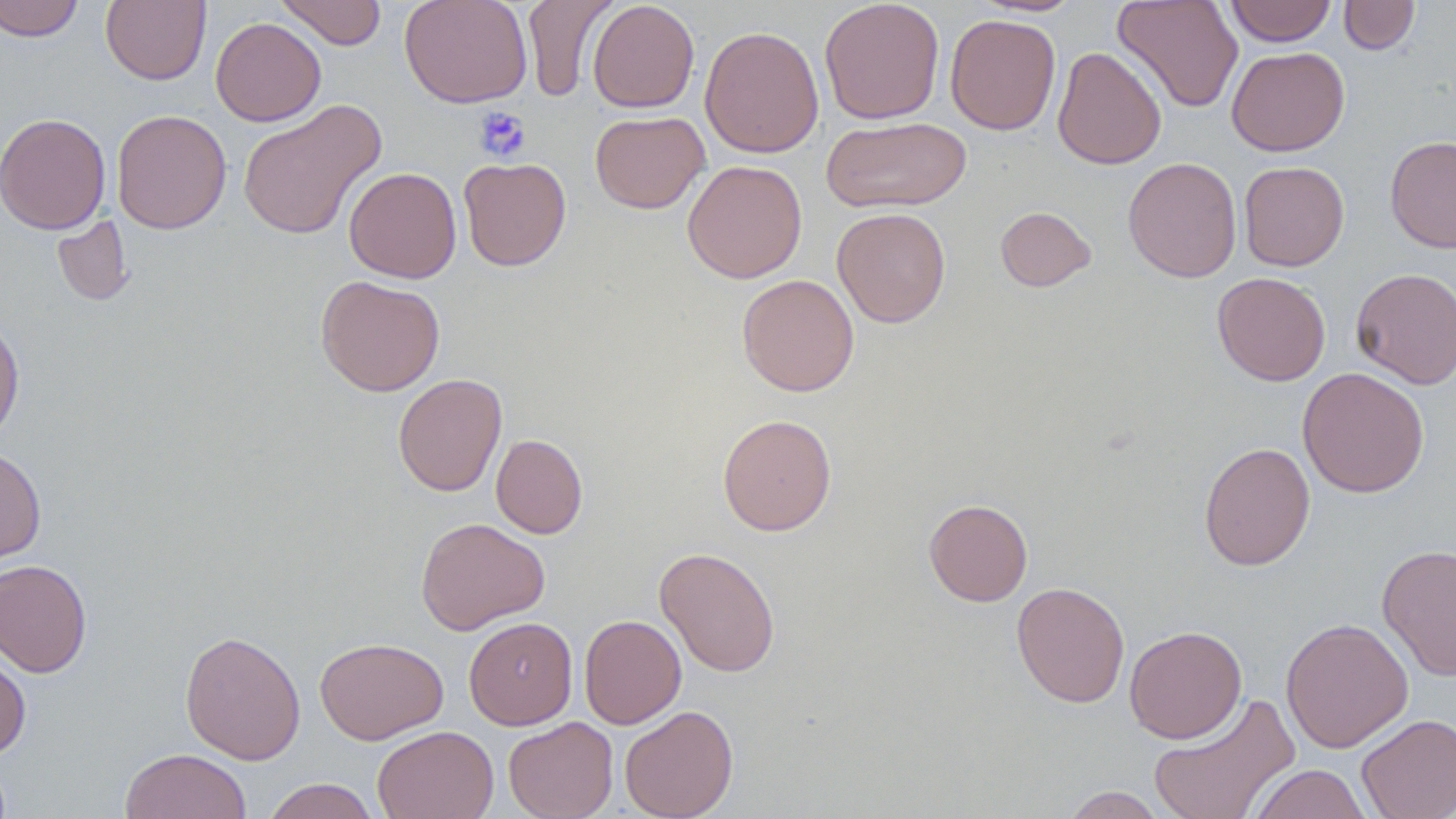

Summary:
  - Coordinate format: approximate bounding boxes as (x1, y1, x2, y2) in pixels
  - Platelet locations: (474, 106, 530, 163)
  - Uninfected red blood cell locations: (0, 0, 84, 41), (100, 0, 211, 86), (274, 0, 387, 50), (399, 0, 533, 108), (522, 0, 618, 102), (587, 0, 700, 113), (819, 0, 945, 125), (972, 0, 1084, 16), (1113, 0, 1244, 113), (1339, 0, 1420, 55), (1224, 1, 1337, 46), (945, 14, 1060, 135), (210, 17, 326, 126), (699, 25, 824, 159), (1052, 46, 1167, 170), (1226, 46, 1350, 156), (237, 100, 386, 241), (111, 109, 232, 235), (590, 110, 710, 214), (0, 113, 111, 234), (821, 116, 971, 213), (1385, 135, 1456, 253), (458, 156, 571, 271), (1123, 157, 1242, 282), (682, 159, 807, 283), (1238, 161, 1350, 271), (344, 167, 462, 283), (995, 206, 1097, 292), (832, 207, 951, 327), (52, 215, 134, 307), (1351, 267, 1456, 389), (1212, 271, 1331, 386), (736, 274, 860, 397), (315, 275, 445, 396), (0, 316, 25, 446), (1297, 366, 1429, 498), (392, 373, 507, 497), (717, 414, 837, 535), (491, 434, 587, 539), (1198, 441, 1315, 570), (0, 448, 46, 564), (924, 499, 1033, 606), (415, 517, 550, 635), (1377, 543, 1456, 682), (655, 546, 780, 677), (0, 559, 92, 678), (1011, 582, 1130, 708), (579, 614, 686, 729), (463, 617, 577, 730), (1280, 618, 1414, 753), (1124, 625, 1247, 743), (180, 629, 306, 764), (314, 637, 448, 745), (0, 648, 31, 760), (1147, 692, 1300, 819), (619, 704, 739, 819), (1357, 714, 1456, 819), (503, 716, 618, 819), (372, 725, 499, 819), (120, 748, 252, 819), (1248, 764, 1372, 818), (261, 778, 381, 819), (1059, 786, 1168, 819)
  - Slide-level diagnosis: negative for blood parasites
  - Magnification: 1000x
  - Modality: light microscopy
  - Preparation: thin blood smear
  - Stain: May-Grünwald-Giemsa
  - Field of view: single
  - Image size: 1456×819 pixels